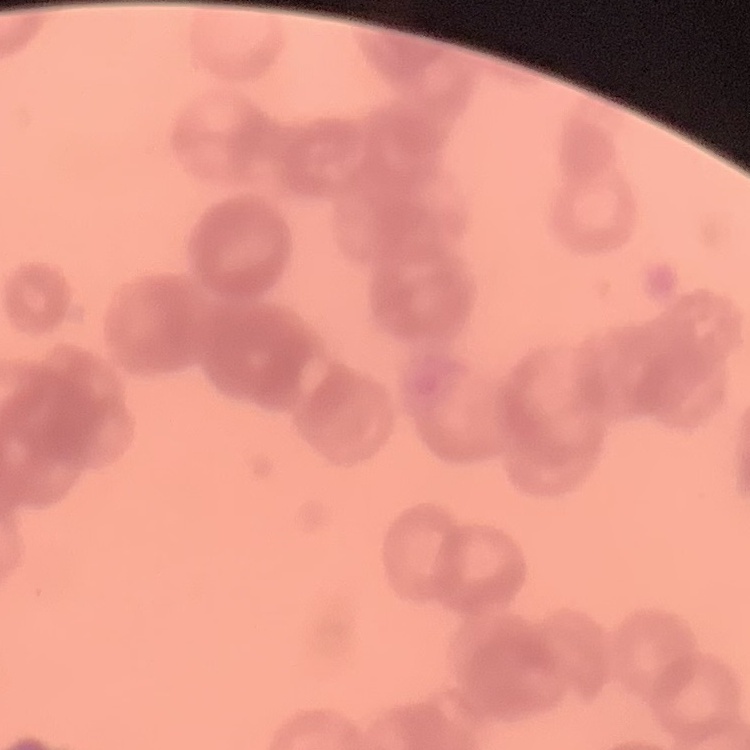

erythrocyte morphology = rouleaux formation
stain = Field's or Giemsa
image type = square crop of a larger photomicrograph
preparation = thin blood film